Identify the parasite.
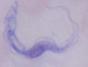

A trypanosome.

Micrograph. Captured at 1000x magnification.